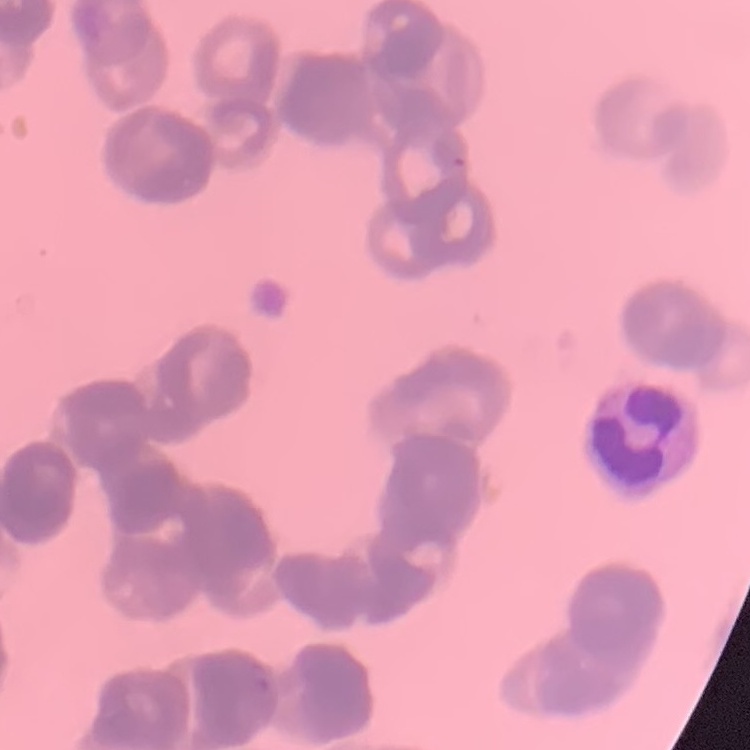

red_blood_cell_morphology: rouleaux formation
preparation: thin peripheral smear
stain: Field's or Giemsa
image_type: one tile cut from a larger photomicrograph